Outline platelets.
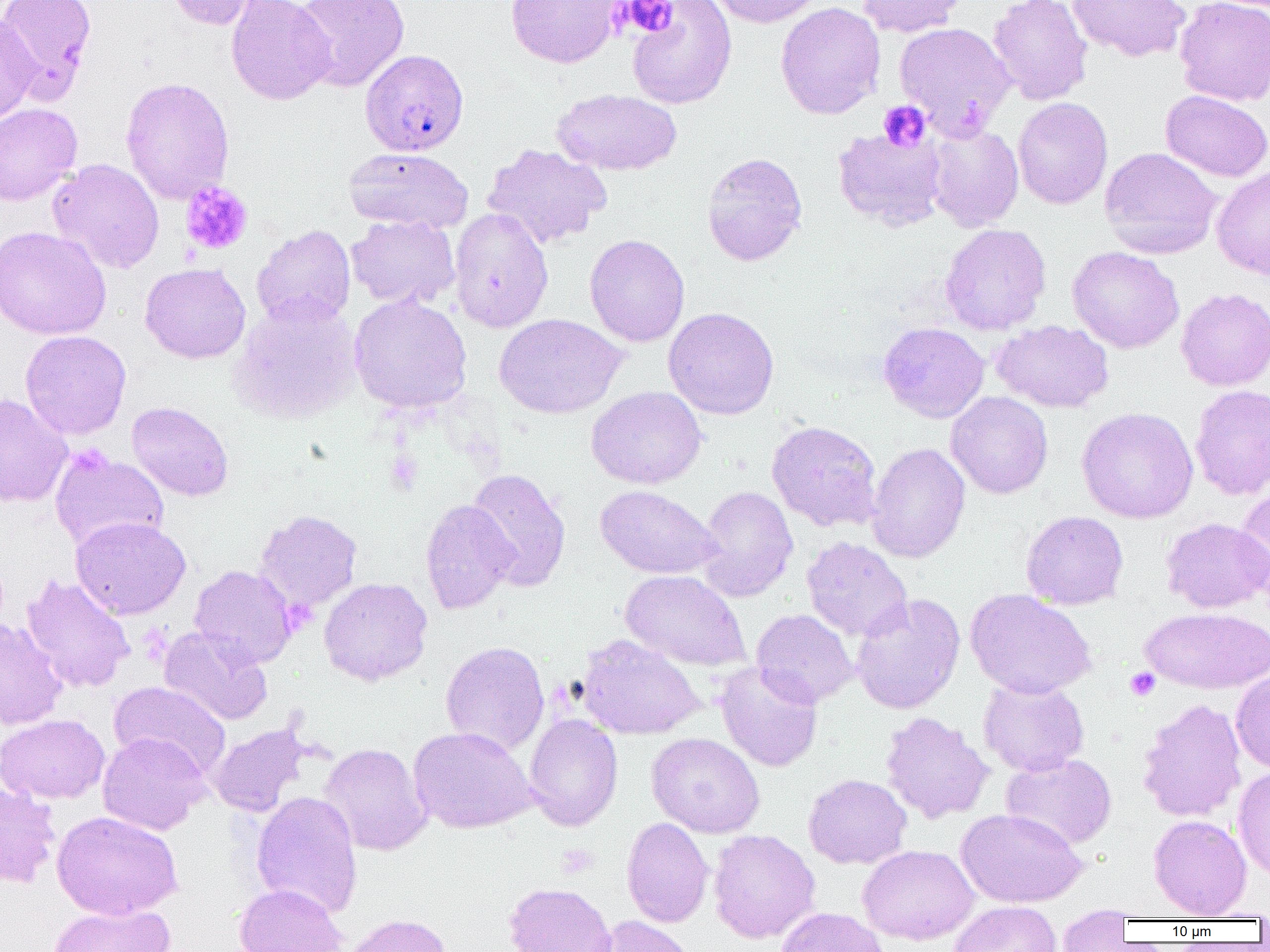

Approximate bounding boxes as [x1, y1, x2, y2] in pixels.
Platelets: [621, 1, 678, 38], [878, 100, 931, 151], [180, 181, 253, 255], [385, 449, 424, 494], [1125, 667, 1160, 701].

Uninfected red blood cell locations: [1, 0, 97, 104], [166, 0, 265, 30], [225, 0, 336, 106], [293, 0, 410, 92], [505, 0, 625, 68], [627, 0, 737, 109], [706, 0, 826, 27], [856, 0, 969, 37], [988, 0, 1093, 105], [1067, 0, 1191, 62], [1174, 0, 1270, 106], [775, 2, 885, 120], [0, 13, 39, 126], [894, 21, 1015, 137], [120, 76, 235, 205], [552, 88, 681, 176], [1160, 90, 1270, 182], [1012, 97, 1112, 209], [0, 103, 82, 205], [924, 123, 1024, 232], [831, 128, 948, 230], [481, 143, 612, 250], [344, 146, 473, 233], [1099, 147, 1222, 258], [701, 152, 808, 266], [47, 158, 165, 274], [1211, 165, 1270, 280], [449, 208, 554, 333], [346, 215, 460, 309], [940, 223, 1051, 335], [252, 225, 356, 329], [0, 226, 111, 340], [584, 234, 690, 347], [1067, 246, 1184, 353], [139, 262, 251, 364], [1176, 287, 1270, 391], [349, 292, 472, 415], [229, 298, 362, 424], [663, 306, 779, 420], [494, 313, 627, 419], [991, 319, 1114, 413], [878, 322, 990, 423], [20, 330, 132, 439], [1190, 384, 1270, 500], [586, 386, 706, 489], [945, 391, 1053, 499], [0, 393, 73, 508], [126, 401, 234, 501], [1076, 407, 1198, 523], [767, 420, 882, 532], [866, 442, 970, 563], [49, 448, 169, 552], [465, 467, 571, 592], [594, 485, 723, 579], [695, 485, 798, 602], [1234, 488, 1270, 602], [420, 499, 518, 615], [254, 509, 363, 613], [1021, 510, 1129, 610], [70, 516, 191, 620], [1161, 517, 1270, 613], [802, 536, 913, 642], [189, 565, 298, 669], [620, 569, 750, 672], [20, 575, 136, 693], [319, 577, 432, 686], [965, 589, 1096, 700], [850, 593, 965, 714], [1140, 606, 1270, 694], [751, 609, 858, 708], [0, 617, 67, 730], [159, 626, 273, 726], [576, 633, 705, 740], [440, 641, 550, 756], [715, 662, 823, 772], [1230, 670, 1270, 773], [978, 677, 1089, 777], [109, 681, 231, 779], [1137, 698, 1247, 822], [880, 712, 994, 824], [524, 713, 623, 832], [1, 714, 110, 804], [207, 723, 310, 817], [408, 726, 536, 834], [97, 732, 210, 835], [646, 732, 765, 838], [319, 743, 432, 855], [1000, 753, 1117, 849], [1232, 766, 1270, 883], [803, 773, 912, 869], [0, 779, 60, 888], [250, 791, 363, 919], [955, 808, 1087, 907], [51, 811, 183, 920], [1148, 815, 1252, 919], [621, 816, 714, 928], [708, 829, 820, 943], [857, 844, 979, 945], [504, 882, 617, 952], [234, 883, 347, 952], [948, 901, 1062, 952], [48, 902, 175, 952], [775, 906, 889, 952], [1057, 909, 1132, 951], [343, 913, 452, 952], [588, 916, 695, 952]. Plasmodium falciparum-infected red blood cell locations: [360, 48, 469, 155]. Slide-level diagnosis: Plasmodium falciparum. Captured at 1000x magnification. Thin blood smear. One field of a larger specimen. Optical microscopy. Image is 1270×952 pixels.